Outline platelets.
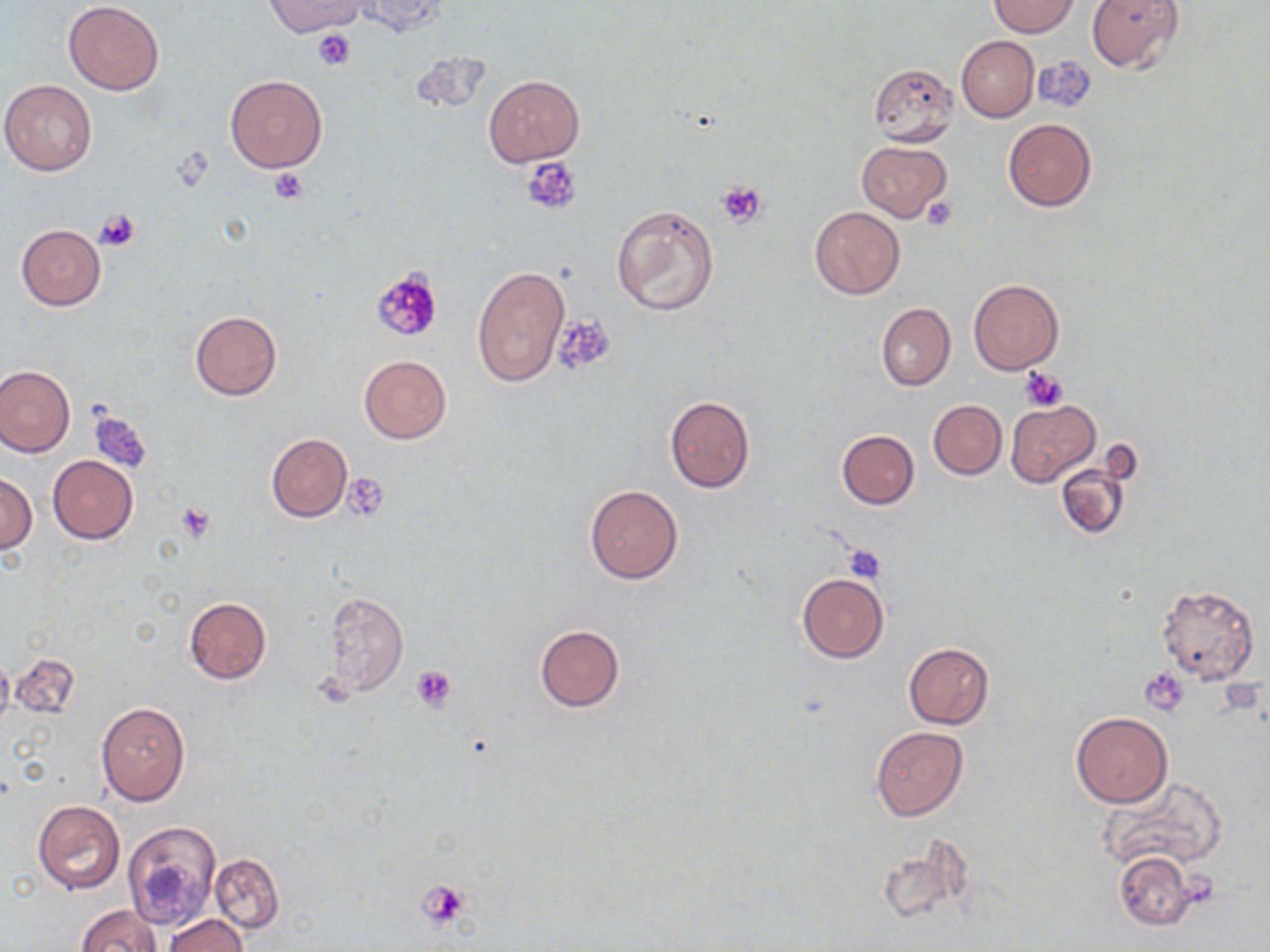

Approximate bounding boxes as named x1/y1/x2/y2 corners in pixels.
Platelets: (x1=312, y1=29, x2=356, y2=70), (x1=522, y1=158, x2=584, y2=215), (x1=270, y1=168, x2=308, y2=205), (x1=716, y1=179, x2=768, y2=227), (x1=921, y1=195, x2=958, y2=230), (x1=93, y1=208, x2=140, y2=252), (x1=371, y1=268, x2=445, y2=342), (x1=552, y1=315, x2=615, y2=376), (x1=1019, y1=367, x2=1068, y2=411), (x1=87, y1=409, x2=152, y2=473), (x1=343, y1=473, x2=389, y2=522), (x1=176, y1=502, x2=219, y2=542), (x1=844, y1=544, x2=888, y2=583), (x1=412, y1=665, x2=457, y2=712), (x1=1141, y1=667, x2=1189, y2=715), (x1=1178, y1=872, x2=1219, y2=910), (x1=417, y1=879, x2=472, y2=930).

slide_level_diagnosis: negative for blood parasites
image_size: 1270×952 pixels
preparation: thin blood film
uninfected_red_blood_cell_locations: 'approximate bounding boxes as named x1/y1/x2/y2 corners in pixels: (x1=265, y1=0, x2=366, y2=36), (x1=350, y1=0, x2=447, y2=35), (x1=1086, y1=0, x2=1184, y2=74), (x1=63, y1=1, x2=164, y2=95), (x1=989, y1=1, x2=1080, y2=37), (x1=956, y1=36, x2=1038, y2=122), (x1=866, y1=62, x2=961, y2=148), (x1=225, y1=75, x2=327, y2=172), (x1=483, y1=76, x2=583, y2=165), (x1=0, y1=79, x2=97, y2=175), (x1=1003, y1=118, x2=1097, y2=212), (x1=856, y1=140, x2=953, y2=221), (x1=610, y1=201, x2=719, y2=318), (x1=810, y1=206, x2=905, y2=298), (x1=16, y1=223, x2=106, y2=310), (x1=471, y1=264, x2=569, y2=387), (x1=969, y1=278, x2=1063, y2=375), (x1=876, y1=303, x2=955, y2=390), (x1=190, y1=310, x2=281, y2=400), (x1=359, y1=354, x2=452, y2=444), (x1=0, y1=363, x2=75, y2=457), (x1=665, y1=396, x2=755, y2=491), (x1=928, y1=400, x2=1006, y2=480), (x1=1007, y1=400, x2=1099, y2=487), (x1=837, y1=430, x2=919, y2=509), (x1=266, y1=433, x2=352, y2=523), (x1=48, y1=456, x2=137, y2=544), (x1=1055, y1=461, x2=1132, y2=540), (x1=0, y1=472, x2=36, y2=554), (x1=584, y1=486, x2=682, y2=583), (x1=797, y1=573, x2=889, y2=662), (x1=1157, y1=585, x2=1259, y2=684), (x1=322, y1=591, x2=408, y2=697), (x1=183, y1=596, x2=271, y2=685), (x1=535, y1=625, x2=624, y2=711), (x1=904, y1=643, x2=994, y2=728), (x1=10, y1=653, x2=81, y2=718), (x1=0, y1=656, x2=14, y2=735), (x1=95, y1=702, x2=191, y2=806), (x1=1070, y1=712, x2=1173, y2=807), (x1=871, y1=726, x2=967, y2=821), (x1=1099, y1=776, x2=1229, y2=875), (x1=31, y1=800, x2=126, y2=895), (x1=123, y1=821, x2=221, y2=930), (x1=881, y1=835, x2=975, y2=927), (x1=1115, y1=850, x2=1194, y2=929), (x1=208, y1=853, x2=284, y2=934), (x1=76, y1=904, x2=162, y2=952), (x1=165, y1=914, x2=248, y2=952)'
field_of_view: single
modality: light microscopy
magnification: 1000x
stain: May-Grünwald-Giemsa